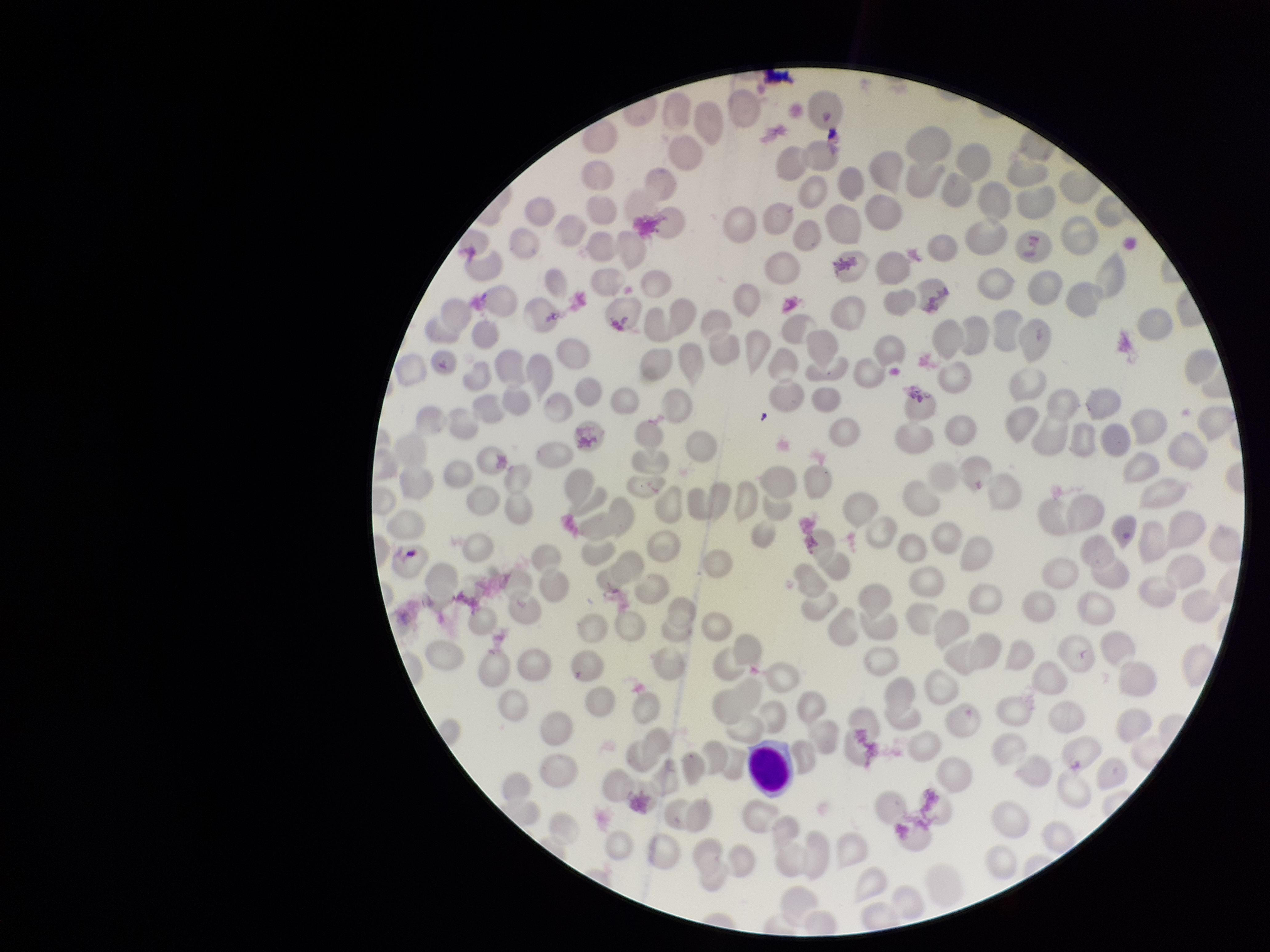

Summary:
  - Image size: 1270×952 pixels
  - Field of view: one from this slide
  - Red blood cell count: 260
  - Patient malaria status: infected
  - Parasitized red blood cells: none identified
  - Parasitized red blood cell count: 0
  - Species reported for this patient: Plasmodium vivax
  - Capture: smartphone photograph through the microscope eyepiece
  - Stain: Giemsa
  - Preparation: thin smear